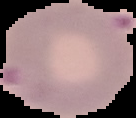

Image is 136×118 pixels. Malaria status: parasitized. From a thin blood smear. The area outside the segmented cell region is set to black.